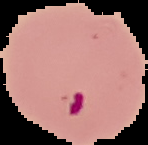

Summary:
  - Preparation: thin blood film
  - Malaria status: parasitized
  - Image size: 148×145 pixels
  - Image type: segmented cell region on a black background